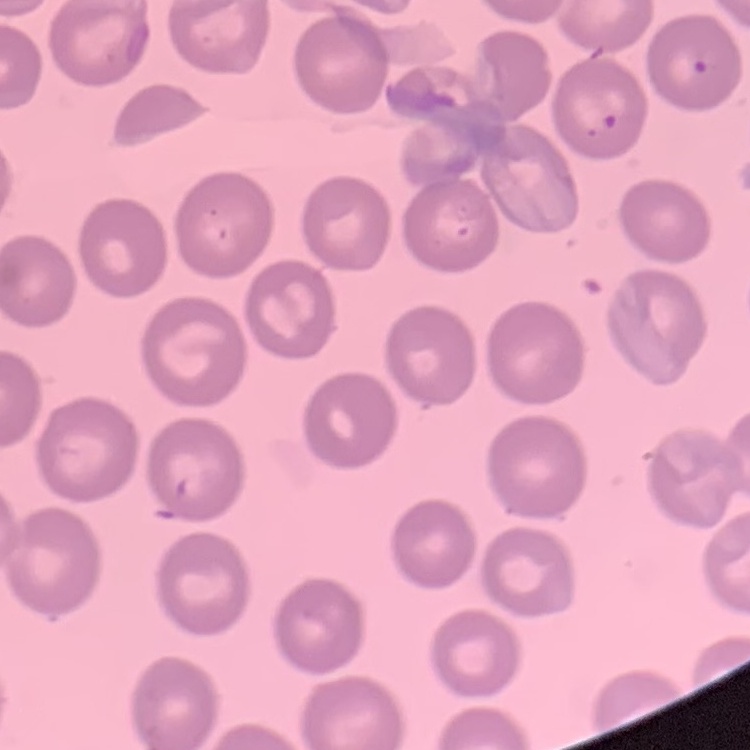

erythrocyte morphology = no rouleaux formation
stain = Field's or Giemsa
preparation = thin blood film
image type = square crop of a larger photomicrograph